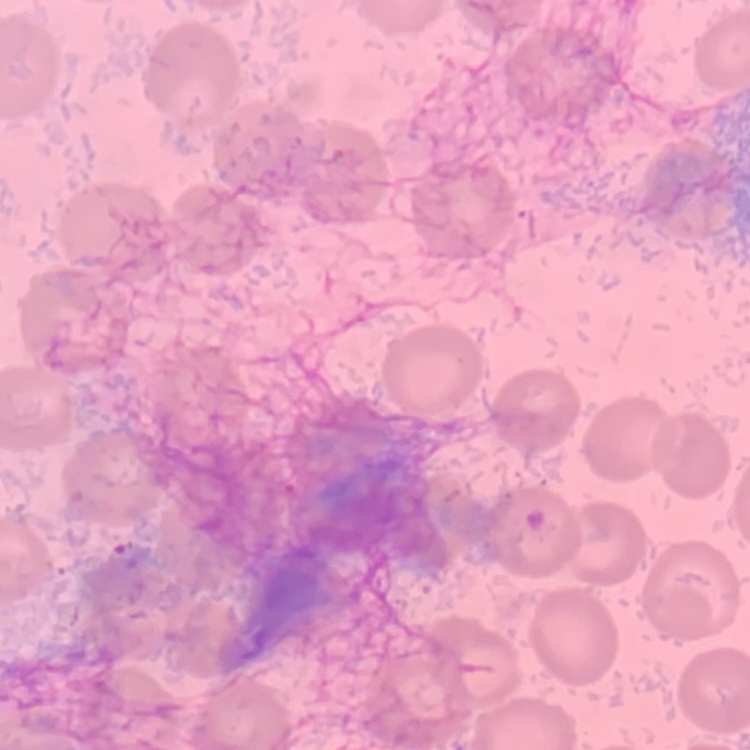

Summary:
  - Red blood cell morphology: no rouleaux formation
  - Preparation: thin peripheral smear
  - Stain: Field's or Giemsa
  - Image type: one tile cut from a larger photomicrograph